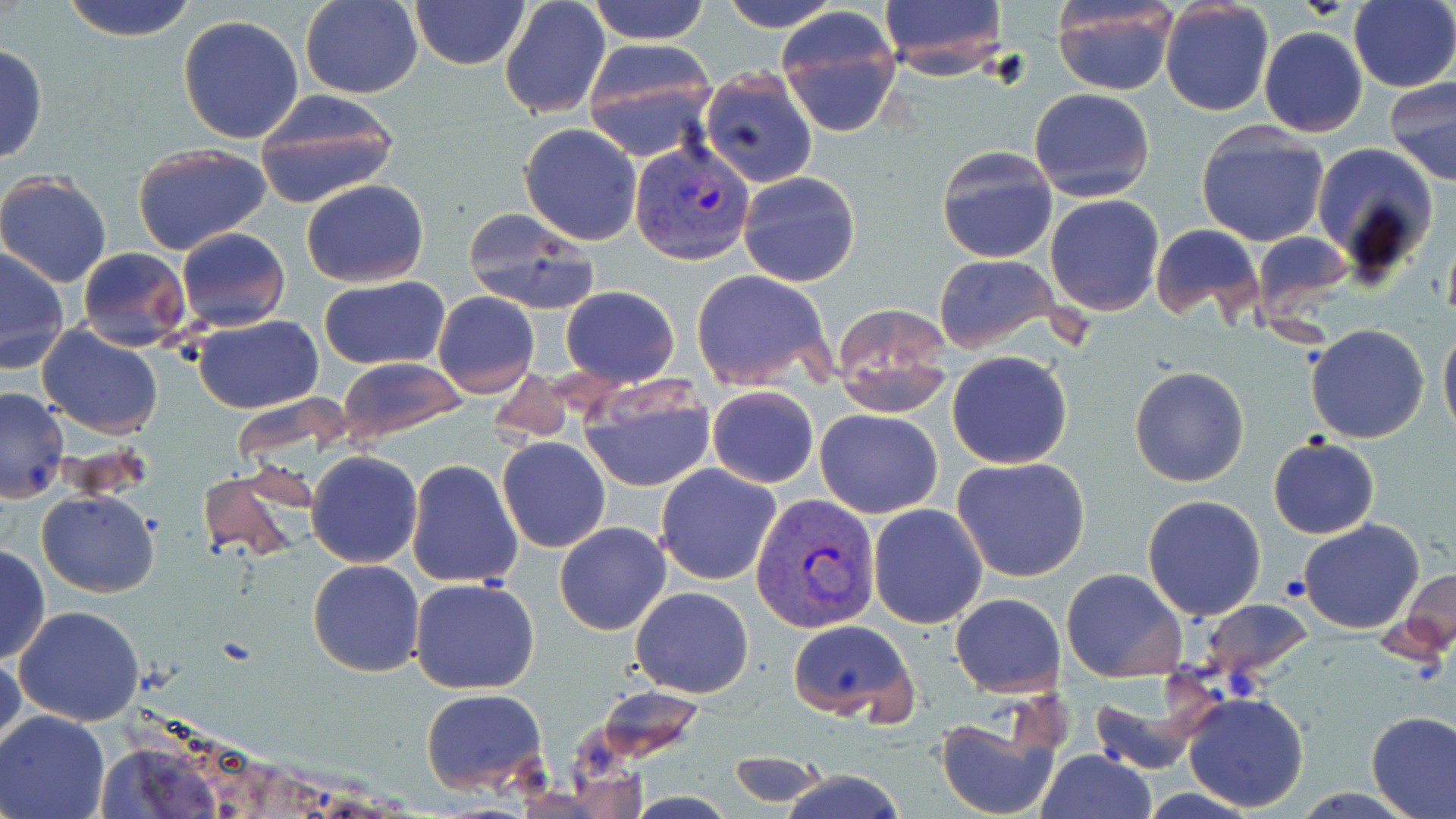
Summary:
  - Coordinate format: approximate bounding boxes as named x1/y1/x2/y2 corners in pixels
  - Plasmodium vivax-infected red blood cell locations: (x1=629, y1=139, x2=756, y2=267), (x1=751, y1=492, x2=881, y2=635)
  - Uninfected red blood cell locations: (x1=60, y1=0, x2=200, y2=43), (x1=299, y1=0, x2=422, y2=98), (x1=409, y1=0, x2=530, y2=69), (x1=499, y1=0, x2=611, y2=120), (x1=587, y1=0, x2=711, y2=44), (x1=713, y1=0, x2=843, y2=30), (x1=876, y1=0, x2=1009, y2=75), (x1=1349, y1=0, x2=1455, y2=92), (x1=1159, y1=2, x2=1275, y2=117), (x1=1050, y1=3, x2=1179, y2=95), (x1=776, y1=7, x2=903, y2=137), (x1=177, y1=14, x2=305, y2=144), (x1=1259, y1=27, x2=1369, y2=137), (x1=580, y1=41, x2=717, y2=158), (x1=0, y1=44, x2=48, y2=165), (x1=698, y1=69, x2=818, y2=188), (x1=1384, y1=76, x2=1456, y2=186), (x1=1028, y1=87, x2=1156, y2=203), (x1=253, y1=91, x2=401, y2=209), (x1=518, y1=122, x2=643, y2=246), (x1=1194, y1=123, x2=1330, y2=247), (x1=1311, y1=141, x2=1438, y2=280), (x1=131, y1=144, x2=271, y2=254), (x1=935, y1=146, x2=1059, y2=264), (x1=738, y1=171, x2=862, y2=286), (x1=0, y1=173, x2=112, y2=287), (x1=301, y1=178, x2=428, y2=287), (x1=1045, y1=193, x2=1165, y2=315), (x1=461, y1=207, x2=600, y2=315), (x1=1149, y1=222, x2=1263, y2=322), (x1=175, y1=227, x2=289, y2=331), (x1=1249, y1=232, x2=1351, y2=317), (x1=76, y1=247, x2=191, y2=351), (x1=0, y1=248, x2=70, y2=374), (x1=933, y1=253, x2=1061, y2=352), (x1=690, y1=268, x2=838, y2=392), (x1=319, y1=276, x2=449, y2=370), (x1=558, y1=286, x2=681, y2=387), (x1=433, y1=292, x2=539, y2=397), (x1=831, y1=303, x2=955, y2=416), (x1=193, y1=315, x2=322, y2=414), (x1=1439, y1=321, x2=1456, y2=446), (x1=1304, y1=323, x2=1431, y2=444), (x1=38, y1=325, x2=163, y2=438), (x1=947, y1=350, x2=1073, y2=469), (x1=338, y1=359, x2=466, y2=442), (x1=1129, y1=366, x2=1250, y2=487), (x1=578, y1=377, x2=715, y2=494), (x1=706, y1=385, x2=818, y2=489), (x1=0, y1=386, x2=70, y2=501), (x1=814, y1=408, x2=944, y2=518), (x1=1267, y1=435, x2=1380, y2=540), (x1=497, y1=436, x2=611, y2=553), (x1=307, y1=451, x2=423, y2=568), (x1=952, y1=456, x2=1091, y2=582), (x1=406, y1=459, x2=524, y2=589), (x1=655, y1=463, x2=782, y2=585), (x1=197, y1=466, x2=311, y2=563), (x1=37, y1=488, x2=159, y2=597), (x1=1142, y1=493, x2=1266, y2=621), (x1=867, y1=504, x2=989, y2=629), (x1=1297, y1=519, x2=1424, y2=634), (x1=555, y1=522, x2=672, y2=635), (x1=0, y1=543, x2=49, y2=664), (x1=308, y1=560, x2=426, y2=677), (x1=1059, y1=566, x2=1188, y2=682), (x1=1403, y1=568, x2=1455, y2=655), (x1=409, y1=577, x2=541, y2=694), (x1=630, y1=586, x2=754, y2=698), (x1=949, y1=592, x2=1065, y2=695), (x1=13, y1=606, x2=145, y2=728), (x1=786, y1=618, x2=919, y2=723), (x1=1, y1=647, x2=24, y2=759), (x1=1085, y1=678, x2=1214, y2=777), (x1=420, y1=688, x2=548, y2=794), (x1=1181, y1=691, x2=1310, y2=810), (x1=1367, y1=710, x2=1456, y2=818), (x1=1, y1=711, x2=110, y2=819), (x1=936, y1=715, x2=1063, y2=819), (x1=727, y1=750, x2=825, y2=808), (x1=1035, y1=750, x2=1159, y2=819), (x1=780, y1=769, x2=909, y2=819)
  - Slide-level diagnosis: Plasmodium vivax
  - Modality: light microscopy
  - Preparation: thin blood smear
  - Image size: 1456×819 pixels
  - Stain: May-Grünwald-Giemsa
  - Field of view: single
  - Magnification: 1000x